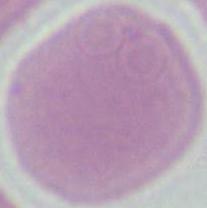 Photomicrograph. 1000x magnification. A red blood cell is shown.